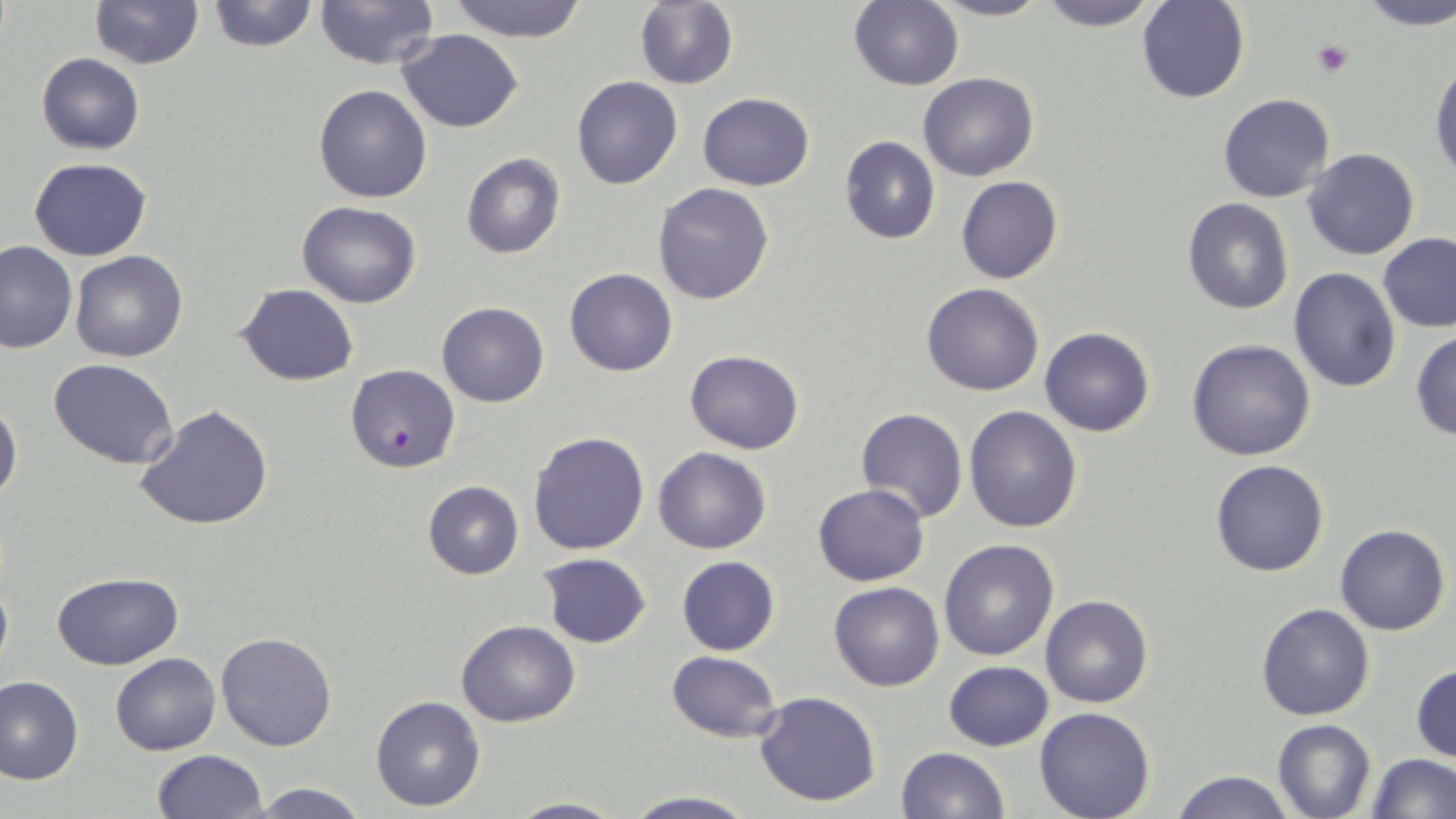
Summary:
  - Coordinate format: approximate bounding boxes as named x1/y1/x2/y2 corners in pixels
  - Platelet locations: (x1=1312, y1=39, x2=1354, y2=78)
  - Uninfected red blood cell locations: (x1=88, y1=0, x2=203, y2=69), (x1=205, y1=0, x2=319, y2=53), (x1=634, y1=0, x2=739, y2=90), (x1=931, y1=0, x2=1051, y2=22), (x1=1035, y1=0, x2=1162, y2=31), (x1=1355, y1=0, x2=1456, y2=29), (x1=314, y1=1, x2=439, y2=70), (x1=444, y1=1, x2=593, y2=42), (x1=848, y1=1, x2=965, y2=91), (x1=1136, y1=1, x2=1250, y2=104), (x1=397, y1=29, x2=522, y2=132), (x1=35, y1=53, x2=145, y2=155), (x1=1430, y1=58, x2=1456, y2=187), (x1=919, y1=71, x2=1038, y2=181), (x1=571, y1=76, x2=683, y2=190), (x1=313, y1=84, x2=432, y2=203), (x1=699, y1=93, x2=815, y2=190), (x1=1219, y1=94, x2=1334, y2=203), (x1=838, y1=137, x2=940, y2=243), (x1=1302, y1=148, x2=1421, y2=260), (x1=461, y1=152, x2=566, y2=259), (x1=29, y1=157, x2=151, y2=261), (x1=956, y1=176, x2=1063, y2=286), (x1=653, y1=183, x2=774, y2=305), (x1=1183, y1=198, x2=1293, y2=314), (x1=296, y1=201, x2=421, y2=308), (x1=1378, y1=233, x2=1456, y2=332), (x1=0, y1=240, x2=75, y2=353), (x1=70, y1=250, x2=190, y2=363), (x1=1287, y1=266, x2=1400, y2=393), (x1=564, y1=268, x2=677, y2=377), (x1=921, y1=283, x2=1045, y2=397), (x1=237, y1=284, x2=358, y2=384), (x1=437, y1=301, x2=549, y2=408), (x1=1039, y1=327, x2=1155, y2=437), (x1=1410, y1=330, x2=1456, y2=440), (x1=1187, y1=339, x2=1315, y2=461), (x1=684, y1=350, x2=805, y2=454), (x1=48, y1=358, x2=179, y2=470), (x1=0, y1=396, x2=22, y2=507), (x1=135, y1=403, x2=275, y2=532), (x1=965, y1=404, x2=1083, y2=534), (x1=855, y1=407, x2=968, y2=524), (x1=528, y1=430, x2=651, y2=556), (x1=653, y1=447, x2=772, y2=555), (x1=1210, y1=459, x2=1329, y2=578), (x1=422, y1=481, x2=524, y2=579), (x1=812, y1=483, x2=929, y2=585), (x1=1335, y1=524, x2=1449, y2=634), (x1=939, y1=538, x2=1059, y2=661), (x1=536, y1=552, x2=652, y2=649), (x1=676, y1=556, x2=780, y2=655), (x1=0, y1=568, x2=13, y2=683), (x1=52, y1=571, x2=183, y2=669), (x1=829, y1=581, x2=944, y2=691), (x1=1040, y1=595, x2=1152, y2=708), (x1=1256, y1=603, x2=1375, y2=720), (x1=456, y1=619, x2=580, y2=727), (x1=216, y1=632, x2=339, y2=751), (x1=666, y1=650, x2=781, y2=743), (x1=110, y1=652, x2=220, y2=755), (x1=944, y1=660, x2=1053, y2=750), (x1=1411, y1=663, x2=1456, y2=763), (x1=0, y1=675, x2=84, y2=785), (x1=753, y1=690, x2=882, y2=807), (x1=370, y1=695, x2=487, y2=811), (x1=1034, y1=708, x2=1156, y2=819), (x1=1271, y1=719, x2=1375, y2=819), (x1=896, y1=746, x2=1009, y2=818), (x1=150, y1=749, x2=268, y2=818), (x1=1367, y1=752, x2=1455, y2=819), (x1=1171, y1=769, x2=1294, y2=819), (x1=247, y1=780, x2=370, y2=818), (x1=620, y1=792, x2=758, y2=819), (x1=501, y1=795, x2=627, y2=818)
  - Plasmodium falciparum-infected red blood cell locations: (x1=346, y1=364, x2=460, y2=475)
  - Slide-level diagnosis: Plasmodium falciparum
  - Stain: May-Grünwald-Giemsa
  - Modality: light microscopy
  - Field of view: single
  - Preparation: thin blood film
  - Magnification: 1000x
  - Image size: 1456×819 pixels